Describe the morphology of the red blood cells.
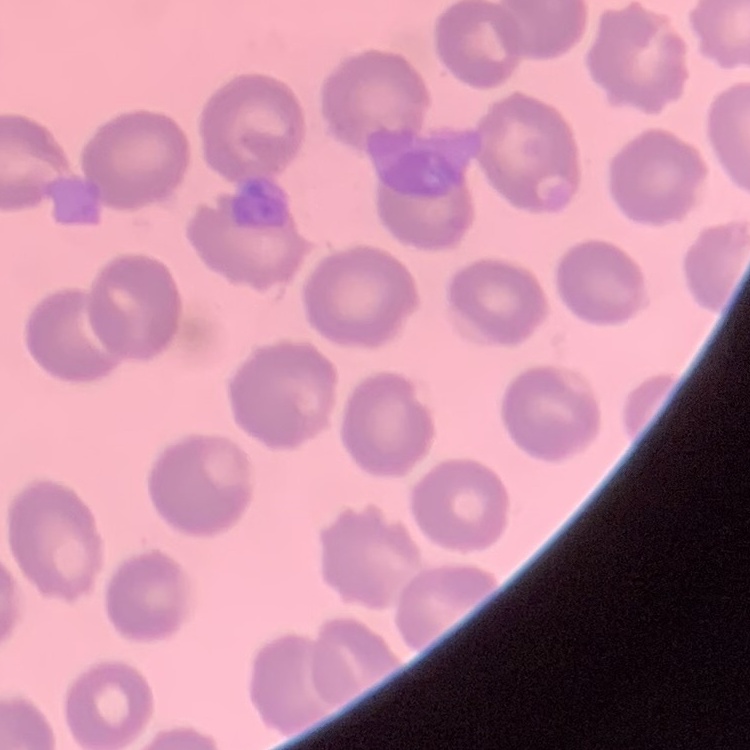

They show no rouleaux formation.

Stained with either Field's or Giemsa. Square crop of a larger photomicrograph. Thin blood smear.